Describe the morphology of the erythrocytes.
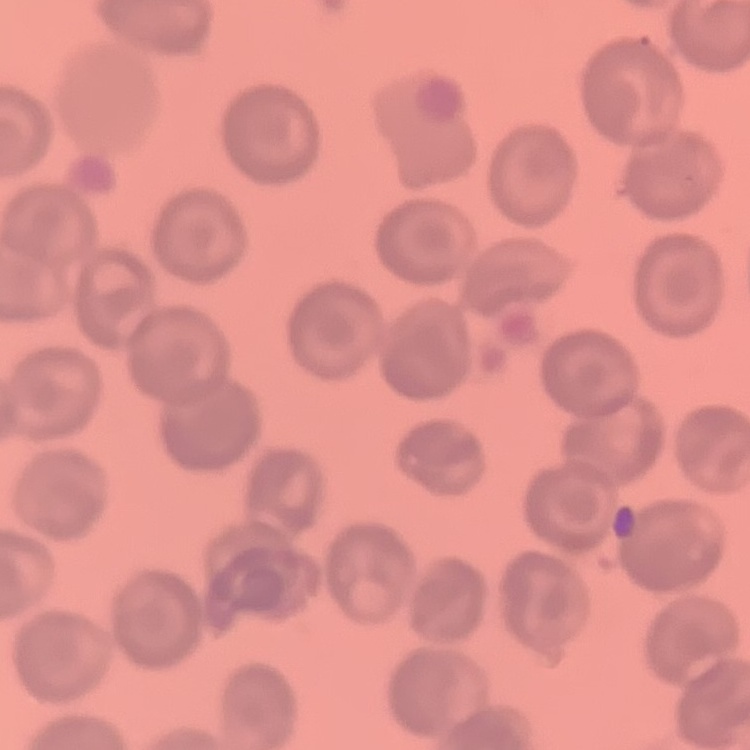

They show no rouleaux formation.

{
  "stain": "Field's or Giemsa",
  "image_type": "square crop of a larger photomicrograph",
  "preparation": "thin blood film"
}